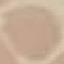

Summary:
  - Malaria status: uninfected
  - Capture: smartphone camera at the microscope eyepiece
  - Image type: automatically extracted cell patch, resized to 64 × 64 pixels
  - Preparation: thin blood film
  - Stain: Giemsa